Give the extent of all uninfected red blood cells.
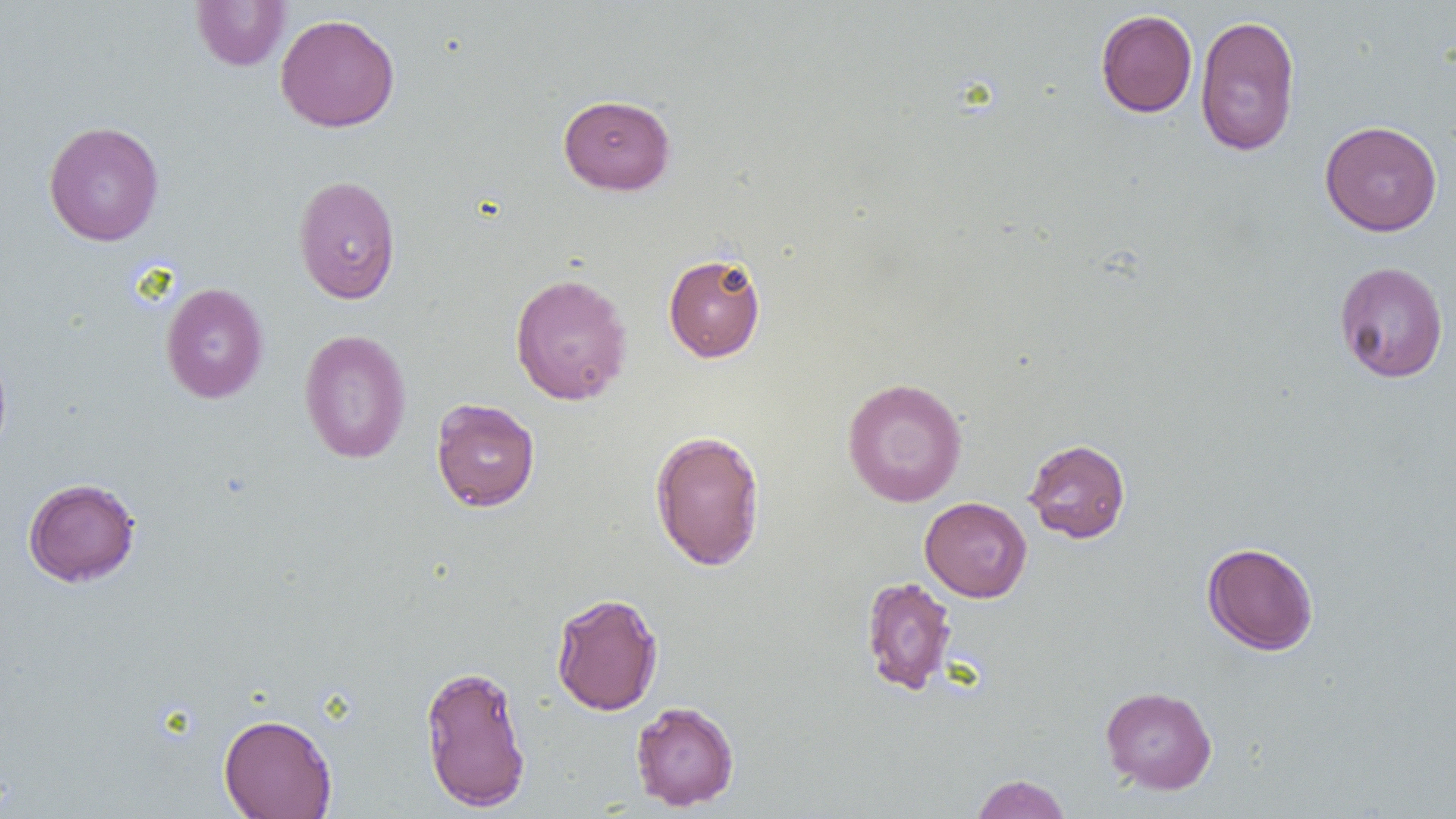

Approximate bounding boxes as (x1, y1, x2, y2) in pixels.
Uninfected red blood cells: (191, 1, 291, 71), (1095, 9, 1198, 118), (275, 13, 400, 133), (1194, 14, 1301, 156), (558, 94, 675, 195), (1319, 120, 1443, 236), (43, 121, 164, 247), (293, 174, 402, 304), (663, 252, 767, 363), (1334, 260, 1449, 383), (509, 273, 633, 405), (160, 283, 268, 404), (298, 329, 412, 464), (0, 344, 13, 463), (842, 377, 968, 507), (431, 398, 540, 512), (650, 429, 766, 571), (1023, 438, 1131, 543), (22, 477, 141, 587), (920, 496, 1032, 602), (1201, 541, 1319, 655), (861, 576, 957, 695), (550, 592, 663, 716), (419, 663, 532, 811), (1100, 686, 1217, 794), (630, 701, 739, 811), (218, 713, 338, 818), (970, 774, 1071, 818).

slide_level_diagnosis: negative for blood parasites
magnification: 1000x
field_of_view: single
image_size: 1456×819 pixels
modality: optical microscopy
preparation: thin blood film